Identify the preparation type.
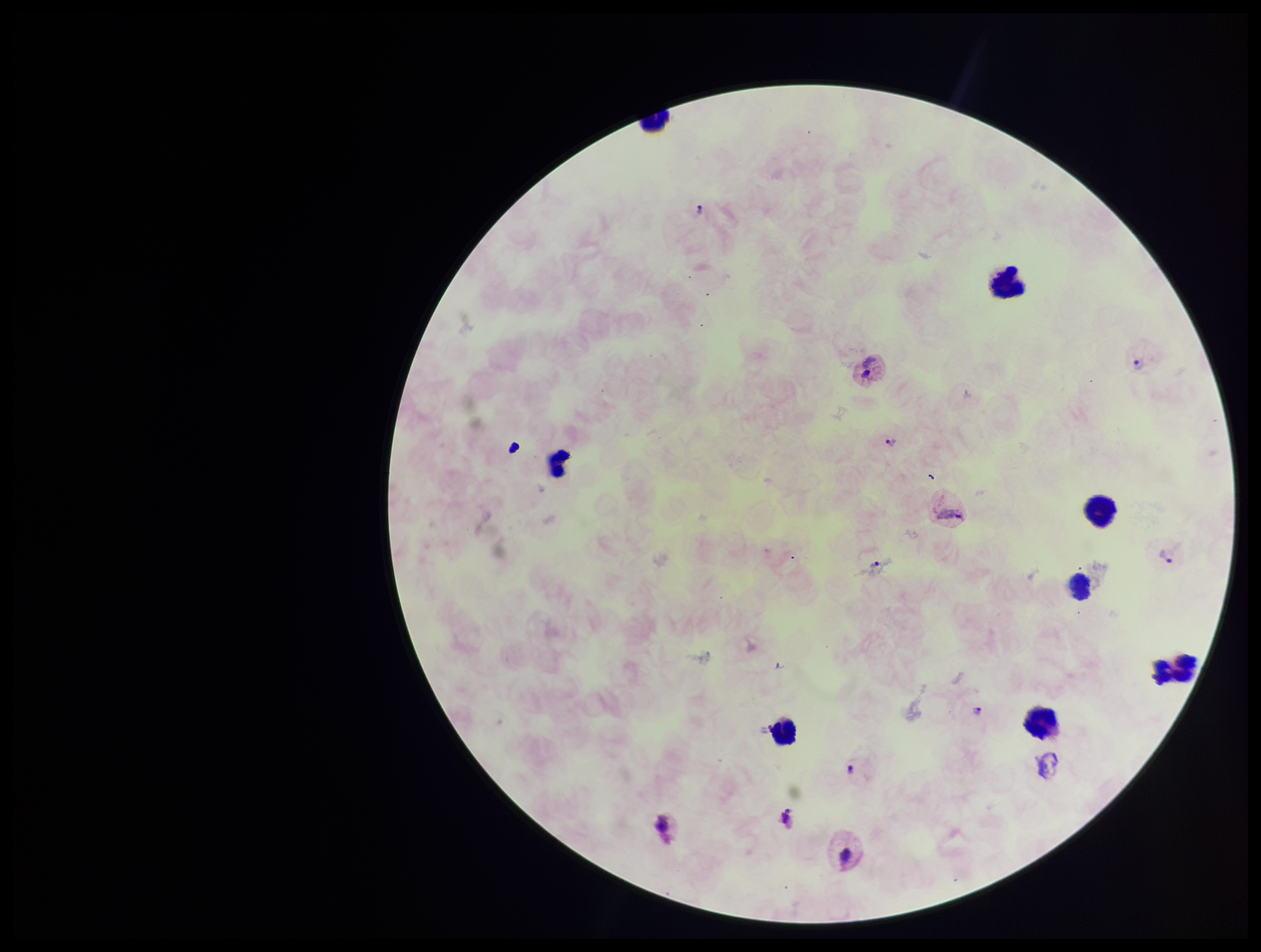
Thick.

Summary:
  - Field of view: one from this slide
  - Species reported for this patient: Plasmodium vivax
  - Stain: Giemsa
  - Leukocyte count: 8
  - Capture: smartphone photograph through the microscope eyepiece
  - Parasite count: 7
  - Image size: 1261×952 pixels
  - Patient malaria status: positive
  - Plasmodium parasites: seen